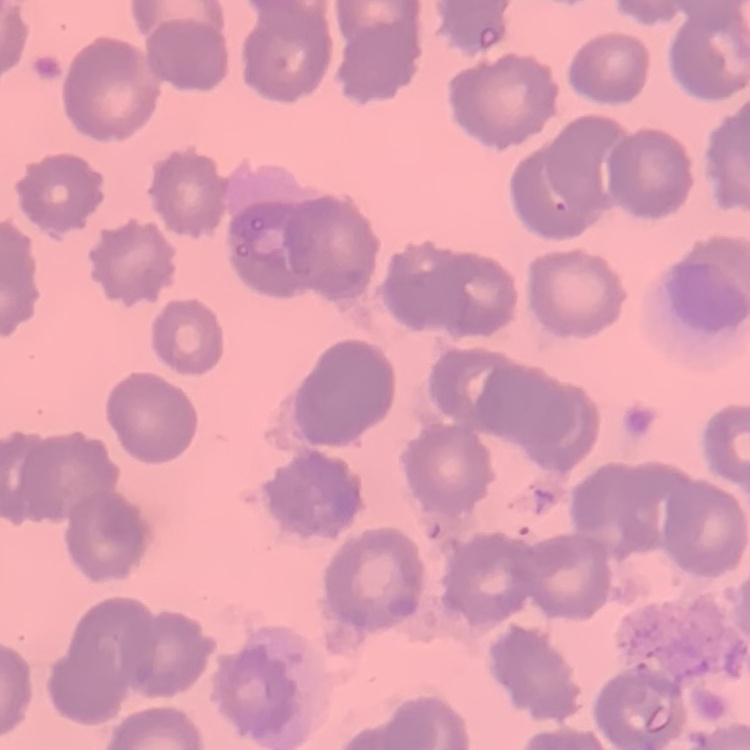
red_blood_cell_morphology: no rouleaux formation
image_type: one tile cut from a larger photomicrograph
preparation: thin peripheral smear
stain: Field's or Giemsa